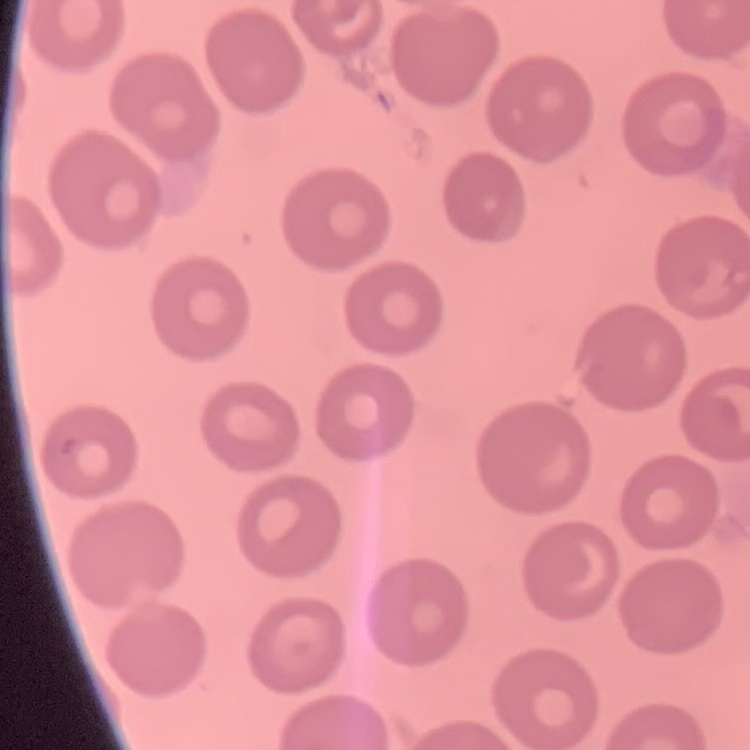

Summary:
  - Red blood cell morphology: no rouleaux formation
  - Stain: Field's or Giemsa
  - Preparation: thin blood film
  - Image type: one tile cut from a larger photomicrograph